Locate every malaria parasite by life-cycle stage, and every leukocyte.
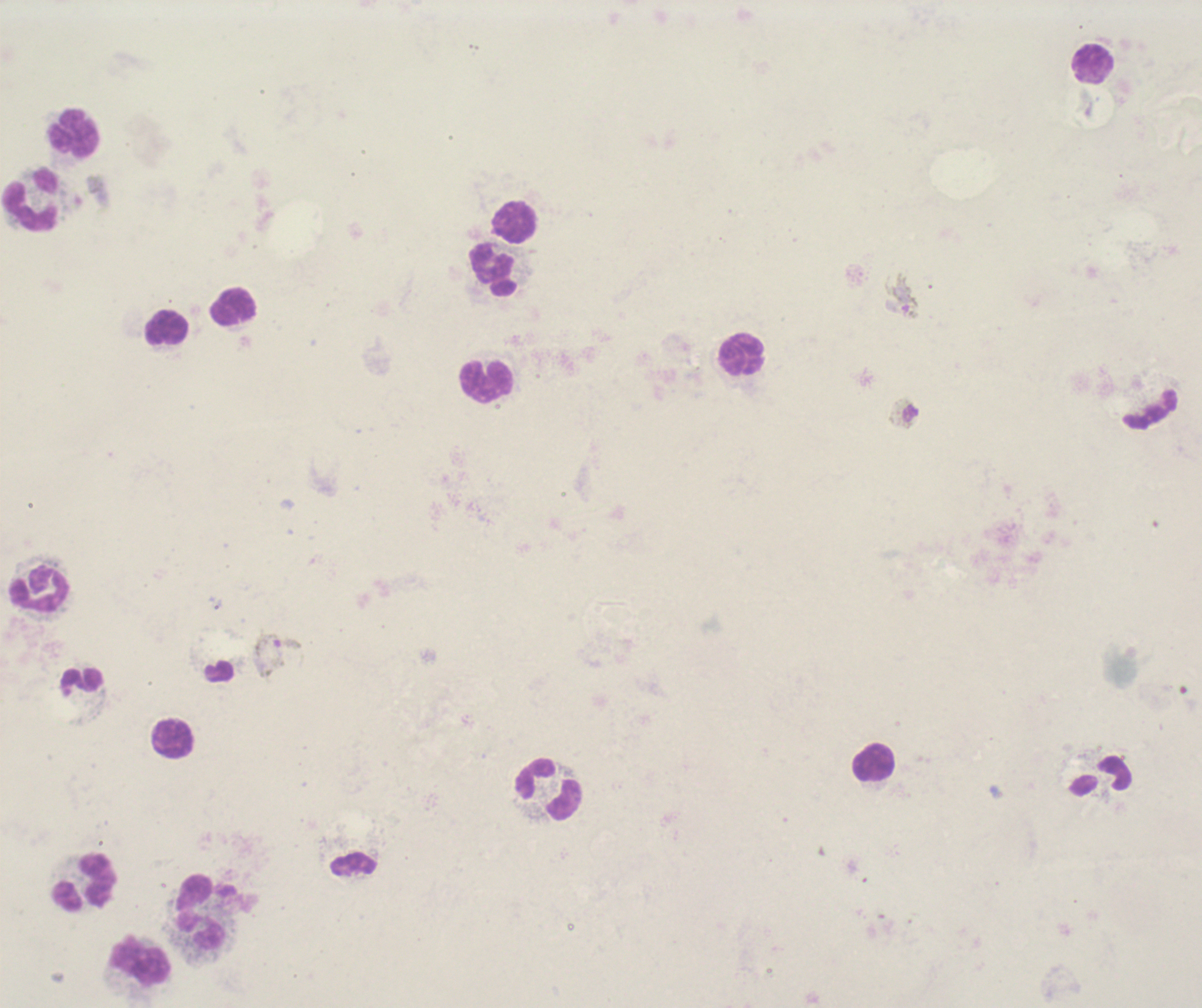

Approximate centers as [x, y] in pixels.
Gametocytes: [902, 297], [903, 413], [278, 655].
No trophozoite or schizont forms observed.
Leukocytes: [1094, 64], [74, 132], [30, 201], [515, 222], [494, 270], [233, 307], [167, 328], [742, 355], [486, 381], [40, 589], [83, 680], [174, 738], [874, 762], [549, 789], [85, 881], [202, 912], [141, 960].

Summary:
  - Background quality: poor
  - Coloration quality: bad
  - Image size: 1202×1008 pixels
  - Stain: Romanowsky
  - Preparation: thick blood film
  - Context: previously used in an actual diagnosis
  - Field of view: one from this slide
  - Magnification: 100x